Assess this cell for malaria.
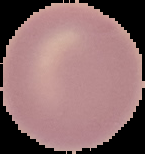
Uninfected.

From a thin blood film. Segmented cell region on a black background. Image is 145×154 pixels.